Report the malaria status of this cell.
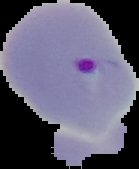

Parasitized.

Summary:
  - Preparation: thin blood film
  - Image size: 139×169 pixels
  - Image type: segmented cell region on a black background